Locate and identify every blood parasite.
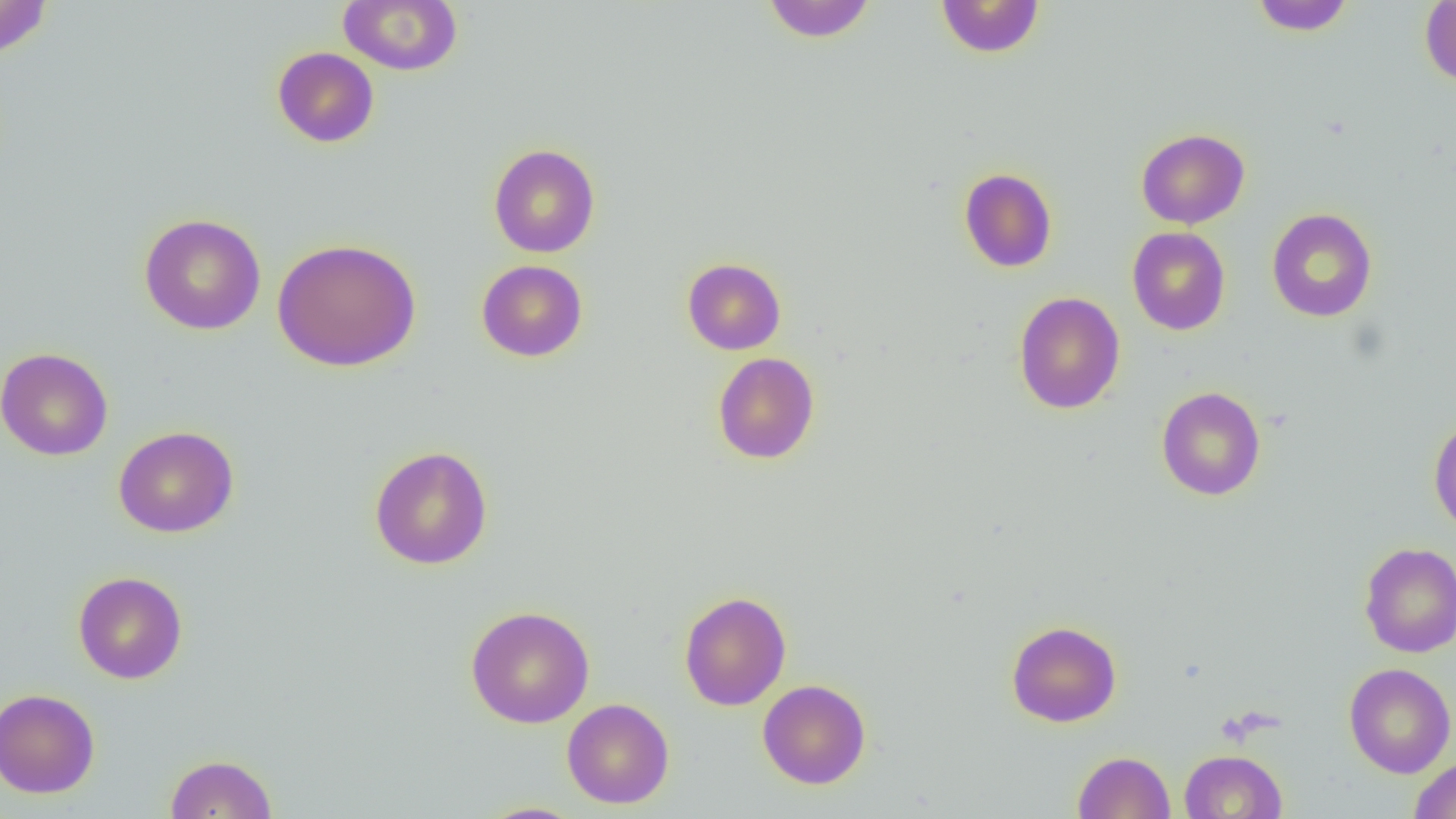
No blood parasites seen.

{
  "slide_level_diagnosis": "no evidence of blood parasites",
  "image_size": "1456×819 pixels",
  "magnification": "1000x",
  "preparation": "thin blood film",
  "uninfected_red_blood_cell_locations": "approximate bounding boxes as (x1,y1)-(x2,y2) corner pairs in pixels: (0,0)-(53,59), (762,0)-(876,43), (935,0)-(1045,58), (1249,0)-(1356,36), (338,1)-(463,75), (1420,1)-(1456,87), (272,47)-(379,148), (1136,128)-(1250,229), (488,143)-(601,258), (958,167)-(1057,273), (1266,207)-(1377,322), (139,213)-(266,336), (1127,227)-(1231,335), (272,238)-(422,372), (682,257)-(786,355), (476,259)-(588,362), (1013,292)-(1125,414), (0,347)-(113,461), (712,352)-(820,464), (1155,386)-(1266,501), (1428,416)-(1456,535), (114,426)-(239,538), (369,445)-(493,570), (1359,541)-(1456,658), (73,571)-(187,684), (679,591)-(792,711), (465,605)-(595,728), (1006,620)-(1121,727), (1343,662)-(1456,778), (758,679)-(871,789), (0,688)-(101,798), (561,698)-(674,809), (1180,749)-(1287,818), (1073,751)-(1176,818), (165,753)-(277,818), (1409,755)-(1456,818), (475,802)-(587,819)",
  "modality": "light microscopy",
  "field_of_view": "single"
}